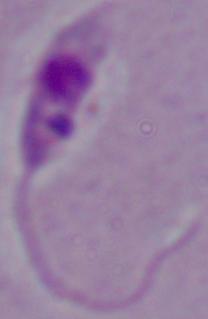

magnification = 1000x
identification = Leishmania
modality = micrograph